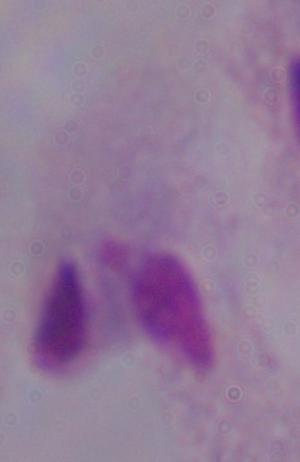

Summary:
  - Magnification: 1000x
  - Identification: trichomonad
  - Modality: micrograph